Locate every blood parasite and identify its species.
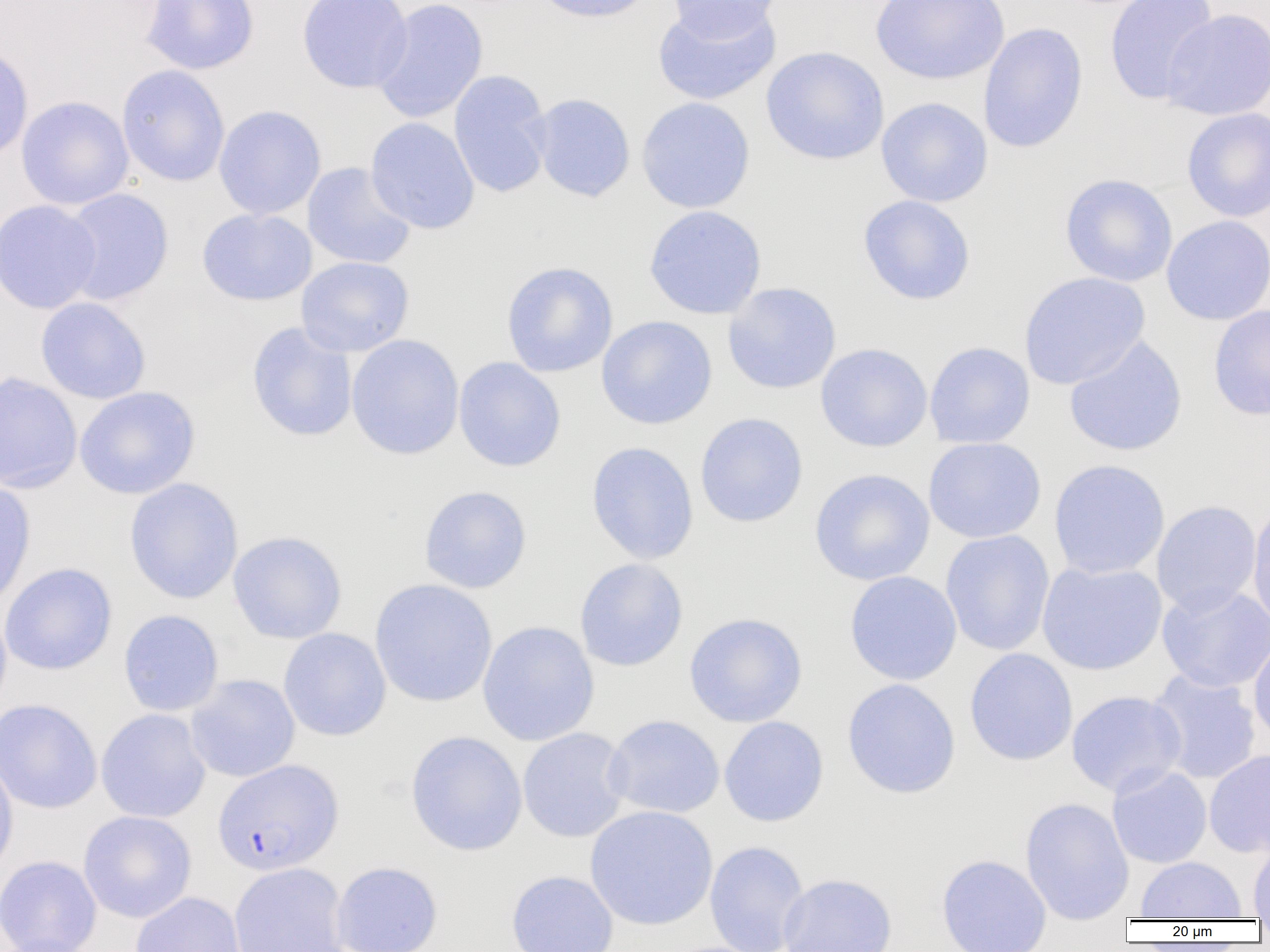
Approximate bounding boxes as [x1, y1, x2, y2] in pixels.
Plasmodium falciparum-infected red blood cells: [213, 759, 344, 876].
No Plasmodium ovale, Plasmodium malariae, Plasmodium vivax, Babesia divergens, or Trypanosoma brucei observed.

slide_level_diagnosis: Plasmodium falciparum
preparation: thin blood film
magnification: 1000x
modality: light microscopy
field_of_view: one of a larger specimen
image_size: 1270×952 pixels
uninfected_red_blood_cell_locations: 'approximate bounding boxes as [x1, y1, x2, y2] in pixels: [140, 0, 260, 75], [297, 0, 413, 93], [371, 0, 488, 123], [531, 0, 657, 23], [665, 0, 782, 42], [869, 0, 1009, 85], [1104, 0, 1220, 104], [652, 2, 781, 106], [1161, 8, 1270, 121], [978, 23, 1088, 153], [0, 44, 34, 163], [760, 46, 889, 165], [116, 65, 230, 186], [448, 70, 553, 198], [529, 93, 635, 203], [16, 95, 134, 210], [636, 97, 755, 213], [875, 97, 993, 207], [213, 105, 327, 220], [1181, 107, 1270, 222], [365, 117, 480, 235], [302, 162, 417, 270], [1059, 174, 1178, 287], [60, 188, 174, 306], [858, 195, 976, 305], [0, 200, 103, 314], [643, 205, 767, 320], [197, 208, 317, 306], [1161, 215, 1270, 325], [296, 256, 415, 357], [501, 261, 618, 378], [1018, 272, 1150, 390], [722, 282, 842, 394], [35, 297, 151, 404], [1208, 304, 1270, 421], [596, 315, 718, 430], [246, 321, 358, 442], [346, 334, 465, 460], [1064, 335, 1188, 457], [923, 342, 1035, 449], [815, 343, 933, 452], [453, 357, 566, 472], [0, 372, 83, 493], [74, 386, 200, 499], [694, 412, 808, 528], [923, 437, 1046, 544], [586, 441, 699, 564], [1048, 458, 1170, 580], [809, 468, 935, 586], [123, 477, 244, 604], [0, 479, 36, 609], [419, 485, 533, 594], [1151, 500, 1262, 616], [1247, 503, 1270, 632], [940, 529, 1055, 656], [227, 530, 347, 643], [574, 558, 689, 672], [1036, 561, 1168, 675], [0, 562, 118, 675], [844, 570, 962, 686], [369, 579, 498, 707], [1157, 583, 1270, 693], [0, 601, 12, 719], [118, 609, 224, 716], [683, 613, 808, 727], [477, 620, 600, 747], [278, 627, 391, 741], [1248, 633, 1270, 747], [964, 648, 1078, 766], [1146, 668, 1262, 785], [185, 674, 301, 783], [841, 678, 961, 799], [1065, 690, 1187, 798], [0, 698, 102, 814], [95, 708, 211, 823], [603, 714, 725, 819], [718, 716, 829, 827], [517, 727, 631, 843], [405, 730, 527, 857], [1203, 749, 1270, 858], [0, 755, 18, 880], [1107, 765, 1213, 869], [1020, 797, 1134, 923], [584, 805, 718, 931], [78, 810, 197, 923], [1247, 839, 1270, 918], [704, 840, 809, 952], [936, 854, 1052, 952], [0, 855, 102, 952], [1135, 856, 1247, 919], [331, 861, 443, 952], [228, 862, 350, 952], [505, 870, 619, 952], [778, 873, 898, 952], [129, 891, 246, 952]'